Classify this cell by malaria status.
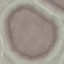

It is uninfected.

image type = cell patch, automatically extracted from a larger field of view and resized to 64 × 64 pixels
stain = Giemsa
preparation = thin blood film
capture = smartphone camera at the microscope eyepiece